Give the position of every Plasmodium parasite.
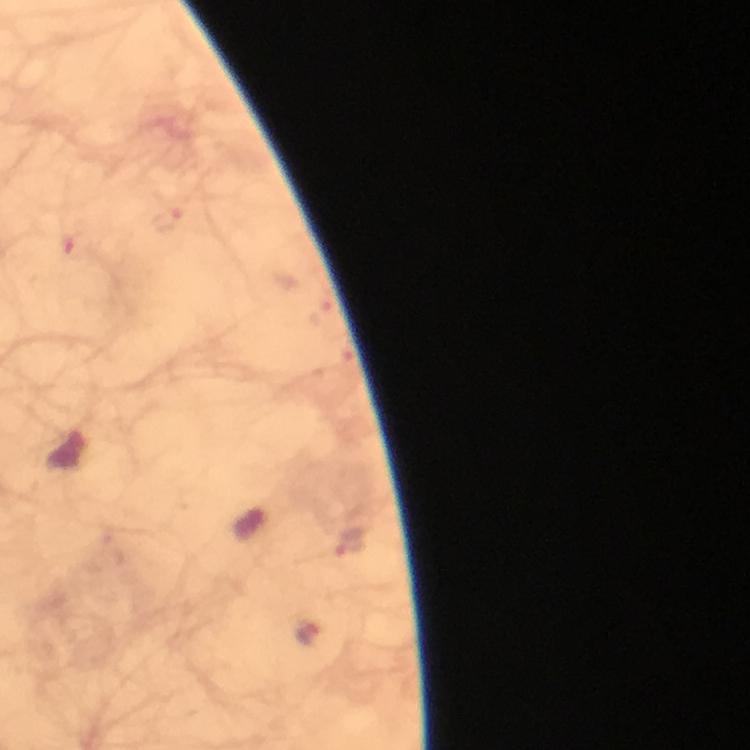

Approximate centers as [x, y] in pixels.
Plasmodium parasites: [167, 219], [76, 247], [349, 544], [308, 633].

Smartphone photograph taken through a microscope. Giemsa-stained preparation. From a diagnostic examination for malaria. Immersion oil applied. Cropped region of a single field of view. Image is 750×750 pixels. 100x magnification. Thick blood smear.